Locate and identify every blood parasite.
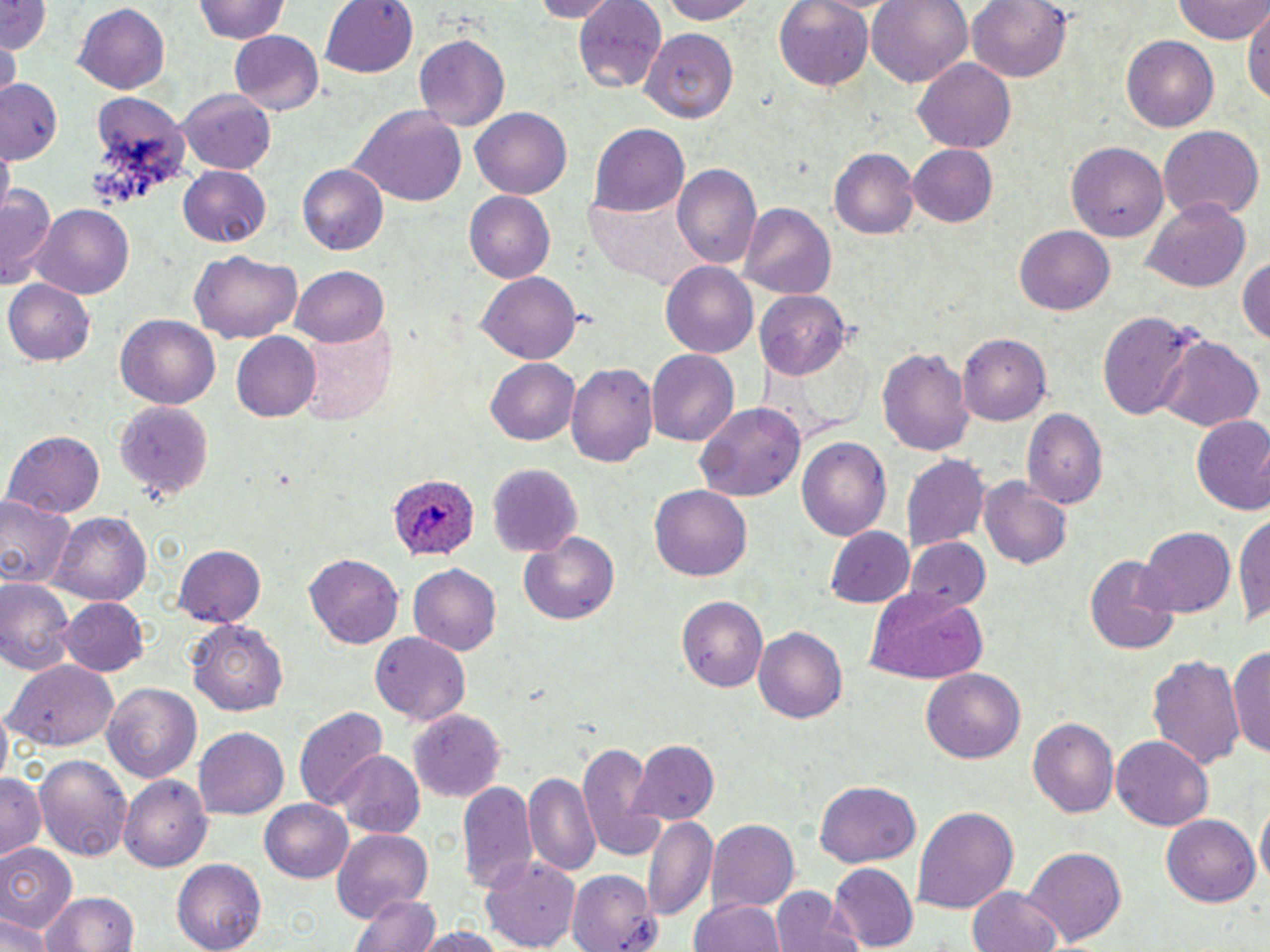

Approximate bounding boxes as [x1, y1, x2, y2] in pixels.
Plasmodium ovale-infected red blood cells: [388, 476, 481, 562].
No Plasmodium falciparum, Plasmodium malariae, Plasmodium vivax, Babesia divergens, or Trypanosoma brucei observed.

slide-level diagnosis = Plasmodium ovale
stain = May-Grünwald-Giemsa
image size = 1270×952 pixels
field of view = single
modality = light microscopy
preparation = thin blood film
magnification = 1000x
uninfected red blood cell locations = approximate bounding boxes as [x1, y1, x2, y2] in pixels: [192, 0, 292, 46], [321, 0, 419, 78], [528, 0, 620, 22], [653, 0, 763, 23], [770, 0, 876, 91], [867, 0, 974, 88], [966, 0, 1074, 83], [0, 1, 51, 53], [574, 1, 669, 87], [1173, 1, 1270, 44], [1242, 3, 1269, 113], [72, 4, 170, 95], [642, 30, 741, 119], [229, 31, 325, 117], [414, 34, 509, 131], [1122, 34, 1219, 132], [3, 41, 20, 95], [911, 59, 1017, 154], [0, 82, 62, 165], [178, 87, 278, 172], [351, 104, 468, 209], [471, 107, 572, 199], [590, 124, 690, 218], [1158, 125, 1263, 220], [1066, 139, 1169, 242], [908, 145, 999, 227], [2, 147, 13, 208], [829, 149, 918, 239], [296, 164, 388, 256], [673, 166, 762, 272], [178, 167, 270, 248], [2, 180, 58, 291], [465, 192, 555, 282], [1141, 200, 1252, 291], [739, 202, 835, 301], [30, 204, 135, 298], [1015, 226, 1114, 314], [191, 252, 301, 344], [1236, 253, 1270, 347], [661, 263, 759, 358], [294, 265, 390, 346], [480, 270, 581, 362], [4, 279, 95, 368], [757, 291, 847, 376], [1094, 310, 1205, 422], [114, 315, 219, 411], [297, 322, 396, 426], [231, 332, 321, 422], [958, 334, 1052, 423], [1156, 334, 1264, 433], [875, 345, 973, 457], [646, 349, 737, 445], [485, 357, 580, 445], [566, 359, 659, 467], [114, 401, 214, 503], [696, 402, 807, 500], [1022, 410, 1106, 509], [1190, 417, 1270, 516], [4, 430, 103, 520], [799, 436, 891, 542], [901, 453, 990, 555], [487, 463, 580, 556], [978, 477, 1073, 570], [650, 486, 750, 581], [0, 495, 77, 591], [1235, 505, 1270, 631], [52, 512, 151, 604], [824, 526, 914, 607], [1138, 527, 1234, 616], [518, 533, 622, 627], [907, 538, 990, 616], [173, 546, 265, 626], [305, 553, 403, 650], [1084, 555, 1179, 655], [407, 564, 500, 658], [0, 577, 76, 676], [864, 589, 990, 683], [676, 597, 768, 694], [60, 598, 149, 678], [187, 620, 289, 717], [754, 626, 848, 726], [371, 634, 469, 727], [1230, 643, 1270, 761], [1148, 652, 1247, 774], [6, 659, 120, 750], [922, 666, 1026, 762], [102, 682, 203, 782], [294, 706, 388, 811], [408, 709, 505, 800], [1027, 716, 1119, 821], [195, 727, 289, 821], [1113, 735, 1213, 830], [575, 740, 667, 861], [629, 740, 719, 825], [332, 752, 422, 837], [33, 753, 134, 864], [524, 770, 601, 879], [1, 771, 44, 860], [121, 773, 210, 870], [458, 779, 541, 896], [814, 780, 921, 868], [261, 797, 355, 883], [1256, 798, 1269, 896], [912, 807, 1017, 913], [1161, 812, 1262, 906], [643, 815, 719, 923], [707, 820, 800, 914], [329, 828, 434, 918], [0, 843, 77, 932], [1024, 845, 1127, 949], [480, 851, 580, 952], [172, 860, 266, 951], [828, 863, 919, 949], [566, 869, 658, 951], [963, 886, 1066, 952], [772, 887, 856, 952], [38, 890, 139, 952], [352, 893, 438, 952], [690, 896, 786, 952], [0, 911, 50, 952], [410, 926, 513, 952]